Report the malaria status of this cell.
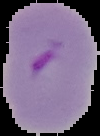

It is parasitized.

image size = 100×136 pixels
preparation = thin blood smear
image type = cell region segmented out of the field of view; surrounding area masked to black